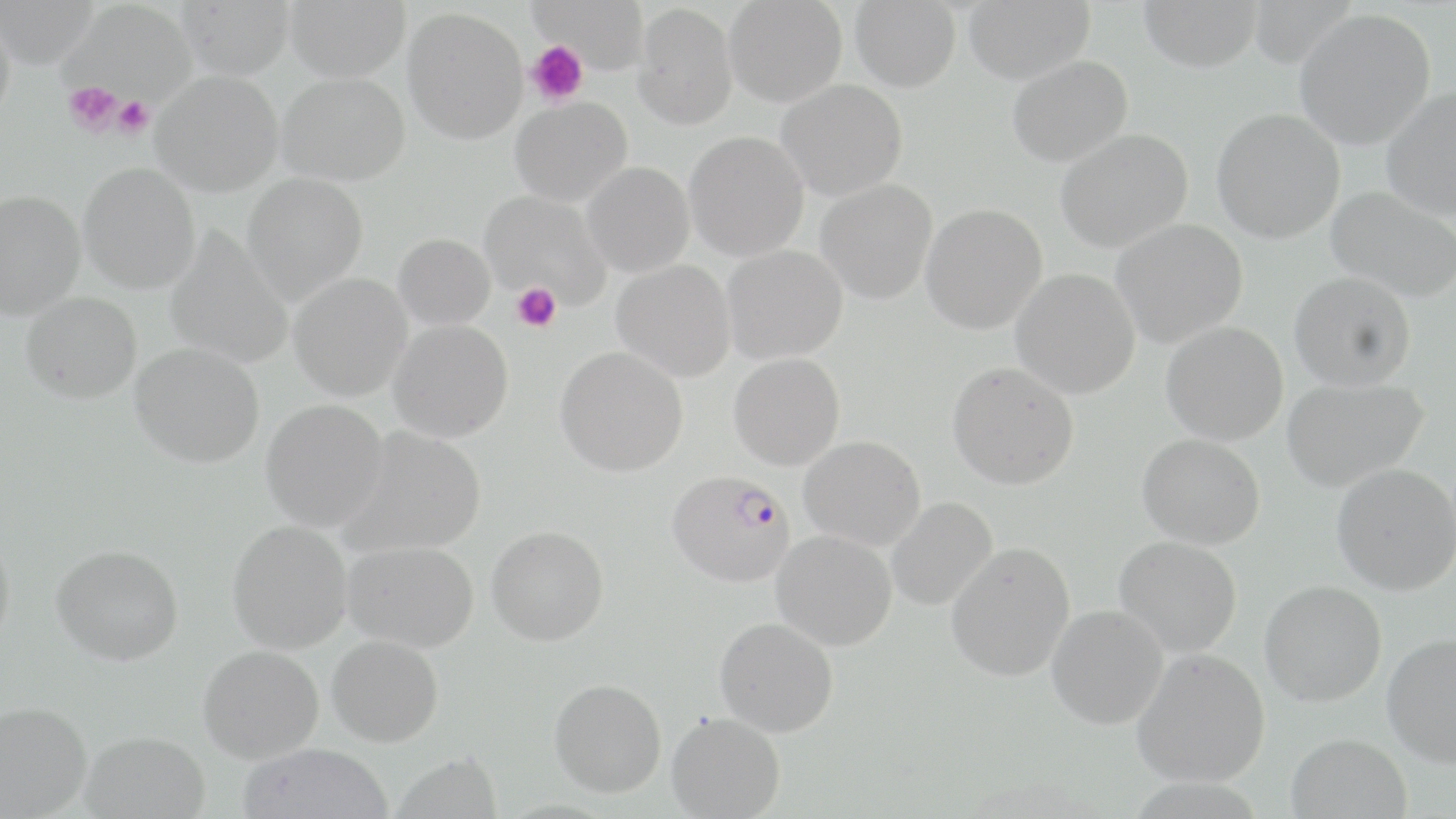 Approximate bounding boxes as (x1,y1)-(x2,y2) corner pairs in pixels. Plasmodium falciparum-infected red blood cell locations: (667,470)-(796,588). Uninfected red blood cell locations: (0,0)-(99,68), (176,0)-(293,80), (284,0)-(409,82), (529,0)-(649,74), (725,0)-(847,107), (850,0)-(960,92), (963,0)-(1095,85), (1138,0)-(1262,72), (66,1)-(196,103), (633,3)-(737,130), (0,8)-(15,129), (403,8)-(528,144), (1294,9)-(1435,149), (1007,55)-(1133,167), (152,71)-(283,196), (277,72)-(409,186), (776,79)-(908,201), (1380,86)-(1456,220), (510,96)-(632,207), (1211,108)-(1345,244), (1054,129)-(1193,253), (684,131)-(809,261), (582,162)-(695,277), (78,163)-(201,294), (242,174)-(367,306), (815,179)-(938,305), (1325,186)-(1455,303), (0,189)-(85,319), (479,190)-(611,309), (920,204)-(1047,335), (1111,218)-(1248,349), (165,228)-(293,370), (392,233)-(496,330), (721,245)-(848,364), (612,260)-(736,383), (1011,269)-(1140,399), (1289,271)-(1416,391), (288,273)-(413,401), (21,292)-(142,404), (388,319)-(514,443), (1161,322)-(1289,446), (129,343)-(265,468), (555,347)-(689,477), (728,353)-(845,470), (947,362)-(1079,490), (1281,377)-(1428,492), (261,398)-(389,532), (339,427)-(488,558), (1137,434)-(1266,549), (799,435)-(926,551), (1331,463)-(1456,595), (886,497)-(998,611), (226,520)-(353,654), (0,525)-(15,655), (486,525)-(609,645), (771,530)-(897,651), (1114,536)-(1242,657), (343,540)-(479,653), (946,541)-(1075,682), (51,545)-(183,665), (1259,580)-(1386,706), (1046,605)-(1168,730), (715,617)-(839,737), (1382,632)-(1456,768), (327,635)-(444,747), (198,645)-(324,764), (1132,648)-(1270,787), (549,678)-(666,798), (0,700)-(92,818), (666,711)-(786,819), (81,731)-(209,819), (1285,733)-(1412,819), (237,743)-(394,819), (390,751)-(503,818). Platelet locations: (526,40)-(587,107), (63,81)-(124,136), (113,96)-(154,138), (512,283)-(562,332). Slide-level diagnosis: Plasmodium falciparum. Thin blood smear. Single field of view. Image is 1456×819 pixels. Optical microscopy. May-Grünwald-Giemsa-stained preparation. 1000x magnification.